Identify the cell.
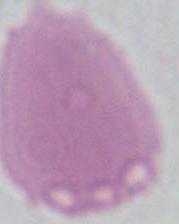

An erythrocyte.

Photomicrograph. 1000x magnification.